Locate every blood parasite and identify its species.
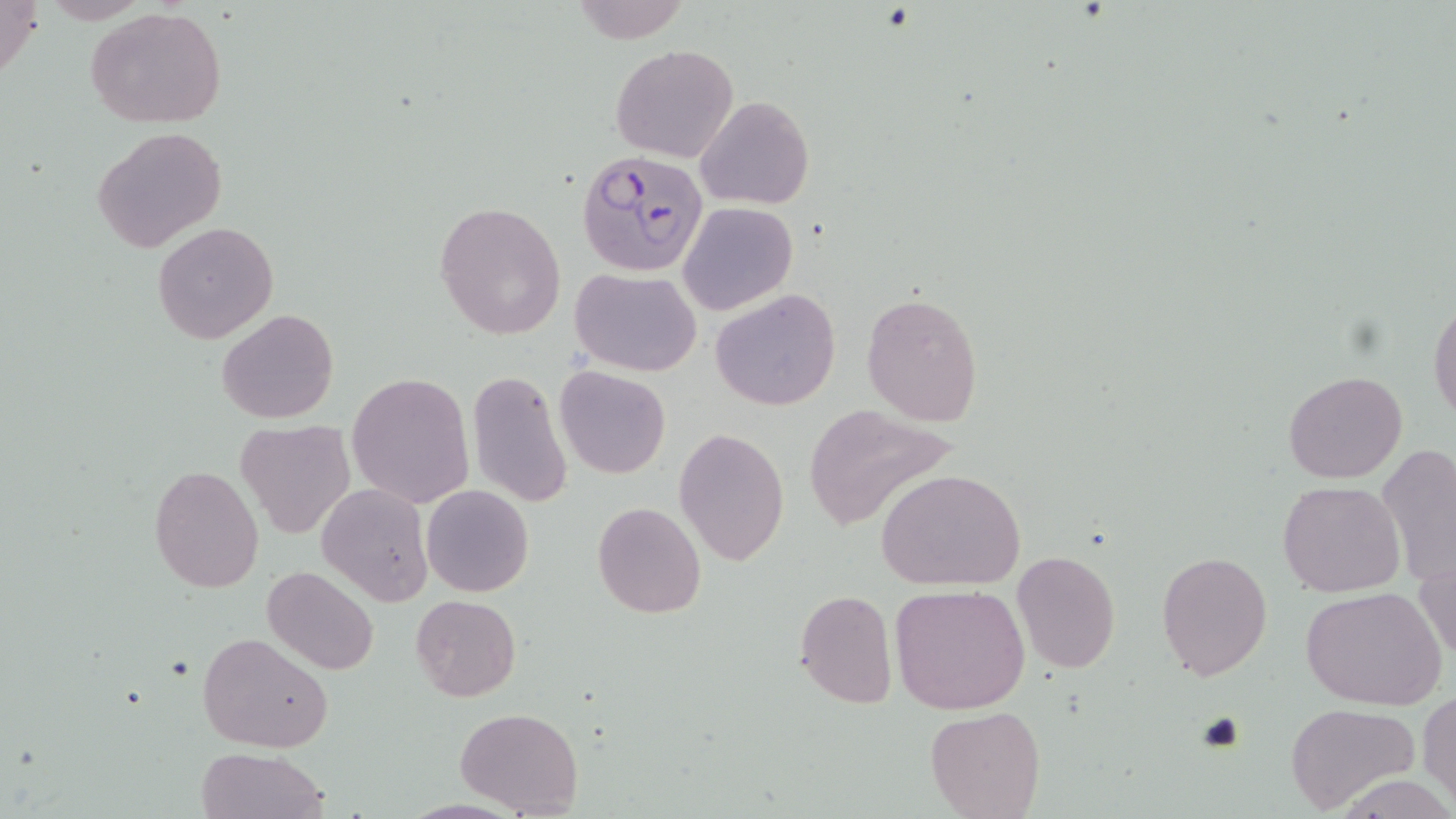
Approximate bounding boxes as [x1, y1, x2, y2] in pixels.
Plasmodium falciparum-infected red blood cells: [575, 150, 710, 278].
No Plasmodium ovale, Plasmodium malariae, Plasmodium vivax, Babesia divergens, or Trypanosoma brucei observed.

slide-level diagnosis = Plasmodium falciparum
magnification = 1000x
image size = 1456×819 pixels
preparation = thin blood smear
field of view = one of a larger specimen
modality = light microscopy
stain = May-Grünwald-Giemsa
uninfected red blood cell locations = approximate bounding boxes as [x1, y1, x2, y2] in pixels: [0, 0, 45, 86], [569, 0, 694, 44], [83, 7, 230, 131], [610, 44, 738, 163], [696, 95, 815, 209], [92, 127, 227, 252], [433, 200, 566, 339], [679, 202, 796, 314], [151, 222, 278, 343], [572, 268, 701, 376], [710, 289, 840, 410], [861, 291, 984, 426], [1429, 298, 1456, 423], [216, 309, 340, 424], [554, 365, 670, 478], [466, 369, 573, 510], [346, 371, 475, 507], [1283, 371, 1407, 484], [800, 403, 963, 532], [238, 419, 355, 540], [674, 426, 791, 566], [1379, 443, 1456, 591], [149, 464, 263, 593], [877, 468, 1026, 590], [1277, 480, 1406, 597], [317, 483, 433, 605], [422, 485, 533, 597], [593, 501, 707, 619], [1414, 542, 1456, 666], [1011, 551, 1121, 675], [1156, 551, 1272, 683], [262, 565, 380, 675], [890, 585, 1030, 715], [1302, 586, 1446, 712], [792, 589, 897, 708], [411, 594, 521, 702], [197, 631, 332, 751], [1418, 692, 1456, 809], [1286, 703, 1420, 814], [926, 706, 1045, 819], [455, 707, 583, 815], [195, 746, 327, 819]